Assess this cell for malaria.
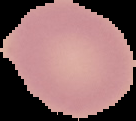

Uninfected.

Image is 136×121 pixels. From a thin blood film. Cell region segmented out of the field of view; the surrounding area is masked to black.